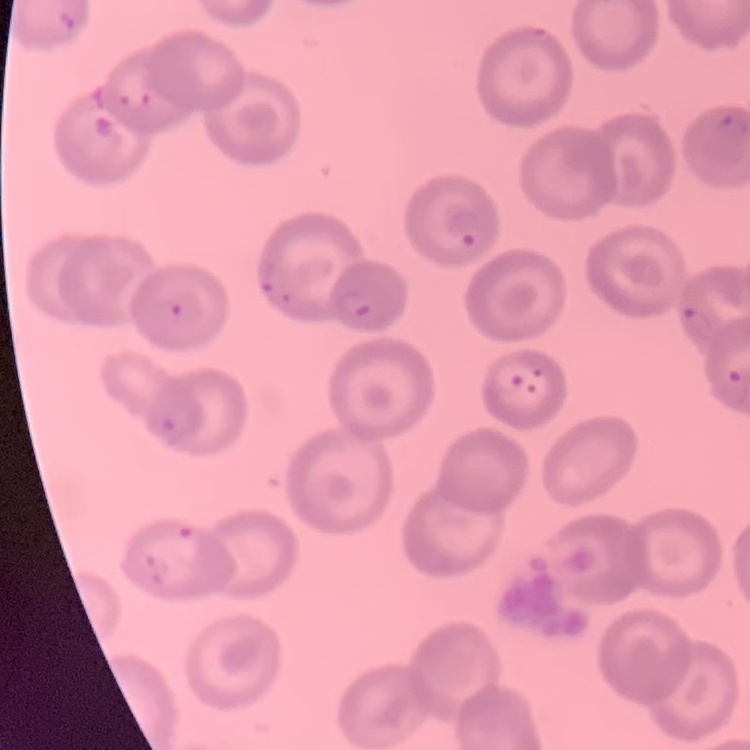

red_blood_cell_morphology: no rouleaux formation
image_type: square crop of a larger photomicrograph
preparation: thin blood smear
stain: Field's or Giemsa